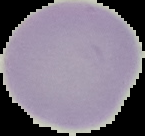
image type = cell region segmented out of the field of view; surrounding area masked to black
malaria status = uninfected
preparation = thin blood film
image size = 145×136 pixels